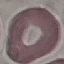
Summary:
  - Malaria status: uninfected
  - Capture: smartphone through the microscope eyepiece
  - Image type: automatically extracted cell patch, resized to 64 × 64 pixels
  - Stain: Giemsa
  - Preparation: thin blood smear